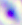 Captured at 400x magnification. Micrograph. Toxoplasma gondii is seen.